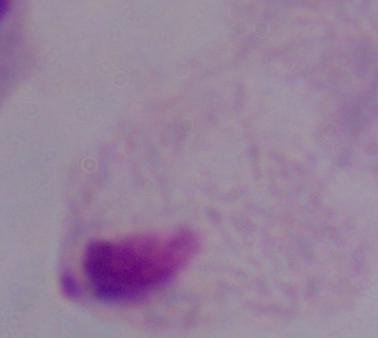

Summary:
  - Magnification: 1000x
  - Identification: trichomonad
  - Modality: photomicrograph